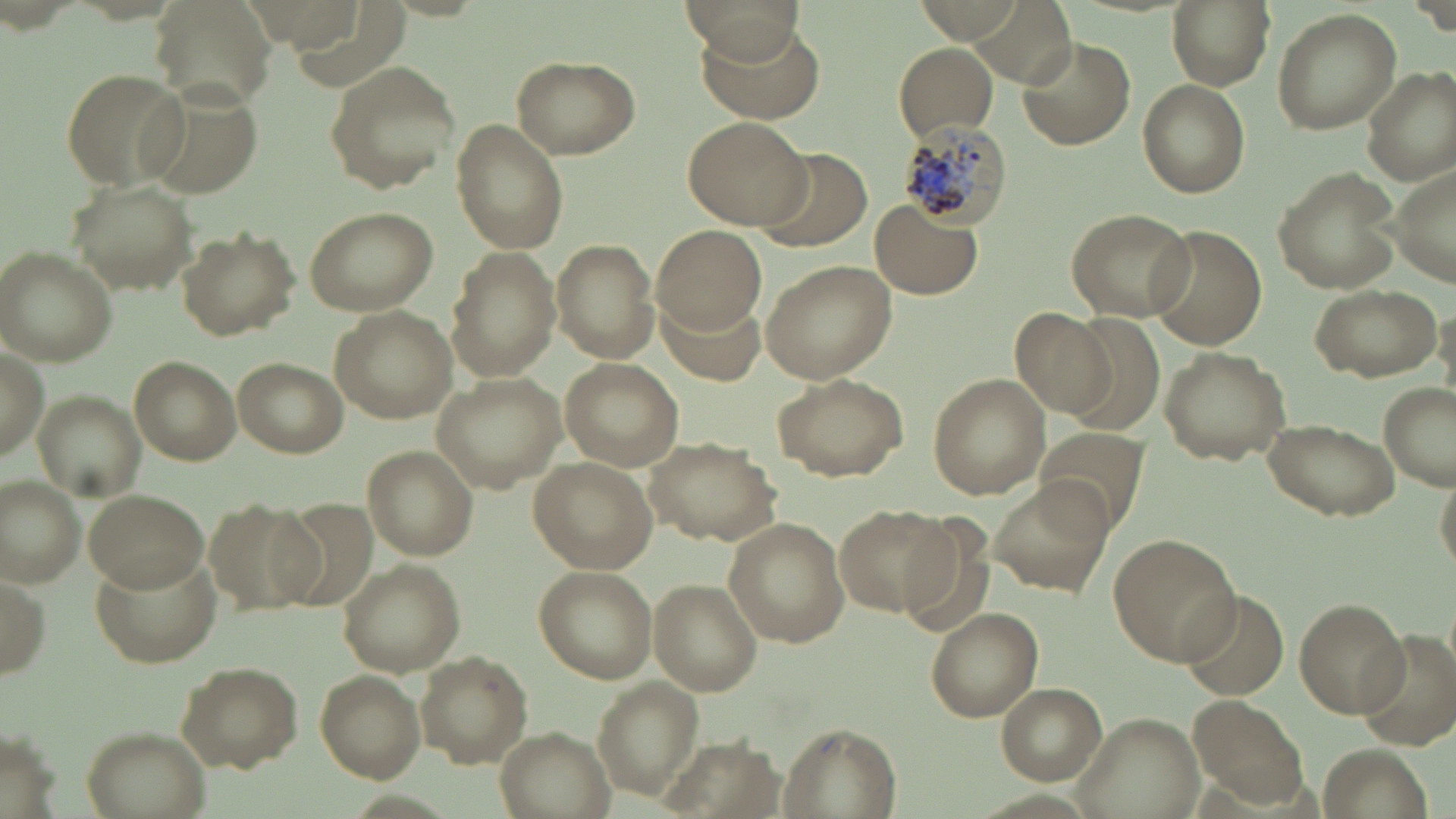

Summary:
  - Coordinate format: approximate bounding boxes as [x1, y1, x2, y2] in pixels
  - Uninfected red blood cell locations: [682, 0, 803, 65], [914, 0, 1024, 43], [1168, 0, 1274, 91], [1271, 8, 1401, 135], [694, 25, 825, 124], [1018, 35, 1135, 150], [894, 44, 1000, 139], [512, 54, 640, 159], [323, 59, 460, 194], [1360, 65, 1456, 184], [59, 67, 188, 189], [1137, 80, 1248, 199], [137, 83, 266, 195], [683, 115, 811, 229], [451, 120, 570, 256], [758, 145, 872, 251], [1381, 159, 1456, 287], [1271, 166, 1402, 295], [68, 179, 194, 295], [869, 200, 984, 299], [300, 205, 439, 316], [1064, 207, 1198, 322], [653, 224, 766, 331], [1146, 225, 1268, 350], [178, 227, 298, 339], [551, 239, 661, 363], [444, 247, 559, 381], [1, 249, 118, 366], [760, 259, 898, 385], [1309, 283, 1441, 380], [656, 293, 768, 386], [329, 306, 454, 422], [1008, 306, 1118, 421], [1, 340, 49, 462], [1156, 346, 1291, 464], [231, 355, 348, 456], [127, 356, 242, 466], [559, 357, 687, 473], [432, 373, 570, 493], [770, 373, 908, 481], [928, 373, 1051, 501], [1378, 382, 1454, 490], [34, 387, 147, 497], [1260, 417, 1401, 521], [1034, 427, 1153, 537], [646, 438, 777, 545], [362, 445, 478, 563], [528, 457, 656, 574], [0, 474, 86, 588], [987, 480, 1112, 601], [83, 488, 206, 590], [205, 496, 323, 615], [835, 504, 955, 617], [722, 516, 850, 648], [1108, 533, 1241, 665], [92, 552, 224, 668], [334, 559, 466, 675], [533, 566, 657, 683], [0, 570, 50, 683], [652, 582, 762, 693], [1175, 589, 1291, 701], [1294, 596, 1408, 717], [924, 608, 1044, 721], [1354, 628, 1456, 749], [415, 651, 532, 767], [173, 659, 304, 770], [314, 670, 425, 783], [592, 677, 707, 802], [995, 684, 1106, 784], [1191, 695, 1308, 805], [1071, 711, 1208, 819], [781, 723, 900, 818], [81, 725, 209, 819], [493, 725, 618, 819]
  - Plasmodium malariae-infected red blood cell locations: [894, 122, 1014, 229]
  - Slide-level diagnosis: Plasmodium malariae
  - Preparation: thin blood smear
  - Field of view: single
  - Modality: light microscopy
  - Image size: 1456×819 pixels
  - Magnification: 1000x
  - Stain: May-Grünwald-Giemsa